Locate the cells, classifying each as a parasitized red blood cell, an uninfected red blood cell, or a white blood cell.
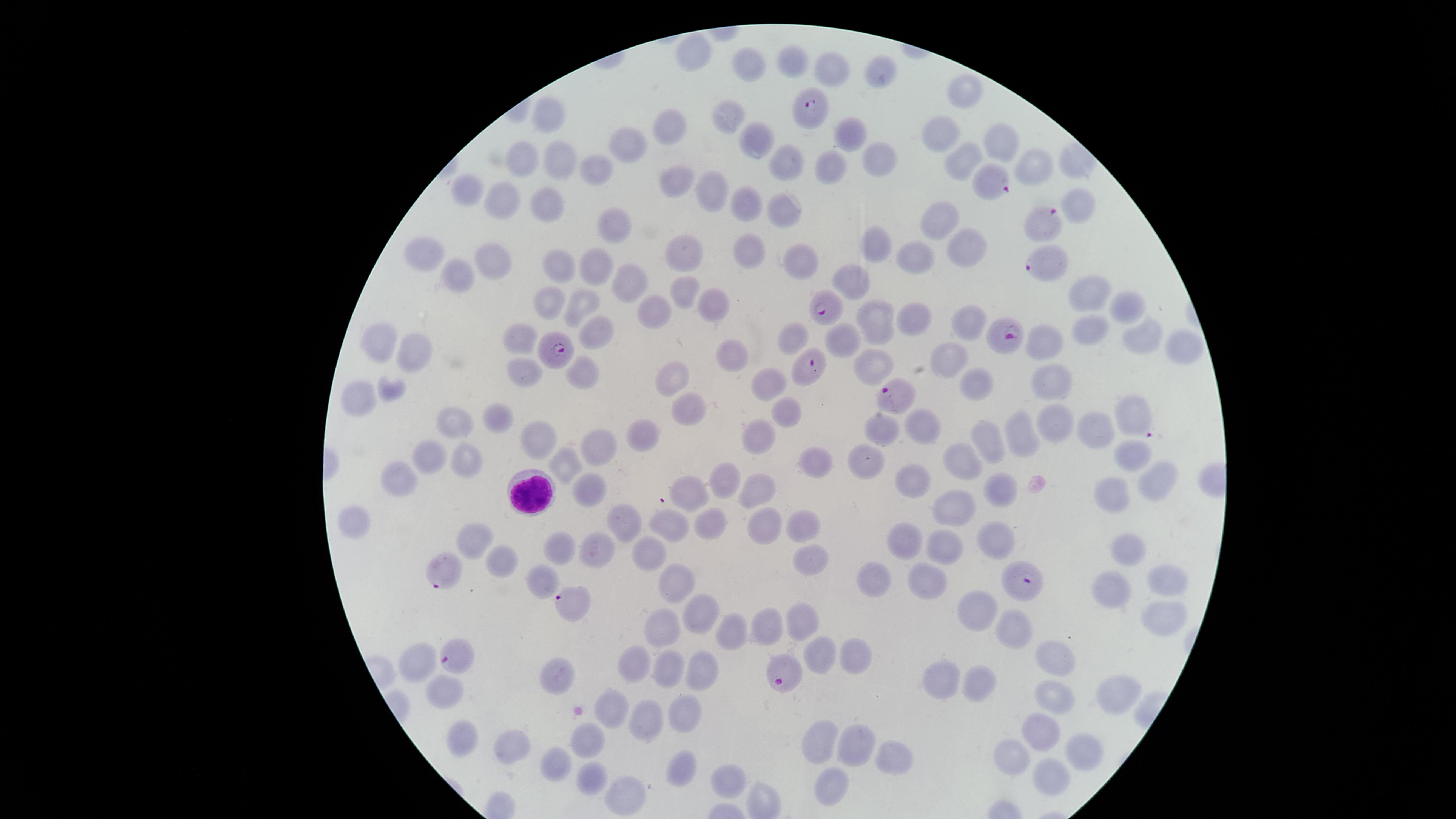

Approximate marker points as {x, y} in pixels.
Parasitized red blood cells: {812, 108}, {992, 184}, {1045, 218}, {1046, 263}, {830, 306}, {1002, 334}, {558, 348}, {805, 365}, {895, 395}, {1134, 414}, {442, 571}, {1018, 579}, {571, 604}, {456, 654}, {786, 673}.
Uninfected red blood cells: {694, 55}, {793, 56}, {741, 64}, {834, 64}, {884, 70}, {968, 90}, {730, 108}, {552, 116}, {672, 124}, {942, 134}, {756, 135}, {854, 135}, {1005, 140}, {631, 142}, {781, 160}, {872, 160}, {962, 160}, {528, 161}, {562, 161}, {601, 162}, {827, 164}, {1036, 164}, {674, 180}, {468, 193}, {712, 195}, {751, 198}, {502, 201}, {546, 206}, {1080, 206}, {790, 207}, {943, 220}, {618, 227}, {878, 243}, {749, 245}, {965, 247}, {684, 253}, {430, 256}, {491, 260}, {800, 262}, {917, 262}, {597, 266}, {557, 272}, {459, 278}, {851, 280}, {630, 282}, {684, 287}, {1090, 292}, {716, 300}, {580, 302}, {547, 303}, {1129, 309}, {654, 313}, {872, 316}, {959, 321}, {914, 322}, {1089, 330}, {599, 331}, {522, 335}, {1141, 336}, {790, 338}, {845, 340}, {382, 341}, {1041, 347}, {1181, 347}, {734, 348}, {414, 352}, {950, 359}, {870, 364}, {520, 368}, {583, 369}, {768, 380}, {1058, 383}, {672, 384}, {978, 386}, {390, 389}, {353, 397}, {684, 410}, {782, 410}, {502, 415}, {460, 420}, {1055, 423}, {879, 426}, {763, 428}, {1093, 430}, {922, 431}, {1018, 433}, {644, 435}, {989, 441}, {603, 444}, {539, 445}, {436, 453}, {1135, 455}, {957, 456}, {464, 457}, {568, 460}, {867, 460}, {811, 462}, {726, 476}, {1159, 477}, {400, 481}, {909, 481}, {1002, 484}, {697, 487}, {762, 489}, {585, 491}, {1109, 494}, {955, 502}, {359, 517}, {807, 521}, {619, 524}, {672, 525}, {770, 525}, {706, 526}, {995, 535}, {482, 536}, {909, 541}, {563, 546}, {949, 546}, {598, 548}, {1124, 548}, {651, 552}, {809, 558}, {503, 565}, {672, 576}, {543, 580}, {922, 580}, {876, 581}, {1169, 582}, {1114, 588}, {984, 607}, {1163, 611}, {696, 613}, {810, 626}, {733, 628}, {1019, 629}, {668, 630}, {763, 630}, {820, 655}, {853, 655}, {423, 659}, {1059, 659}, {636, 661}, {668, 668}, {698, 672}, {559, 675}, {943, 675}, {979, 688}, {1116, 693}, {1057, 695}, {443, 697}, {609, 703}, {684, 712}, {647, 720}, {1045, 731}, {467, 740}, {589, 741}, {855, 743}, {822, 745}, {517, 749}, {887, 755}, {1013, 756}, {1088, 759}, {552, 766}, {687, 771}, {589, 774}, {1051, 776}, {727, 780}, {829, 786}, {618, 795}.
White blood cells: {535, 492}.

preparation = thin blood smear
species = Plasmodium falciparum
capture = smartphone photograph through the microscope eyepiece
image size = 1456×819 pixels
stain = Giemsa
visible region = circular
field of view = single